Rate the background quality.
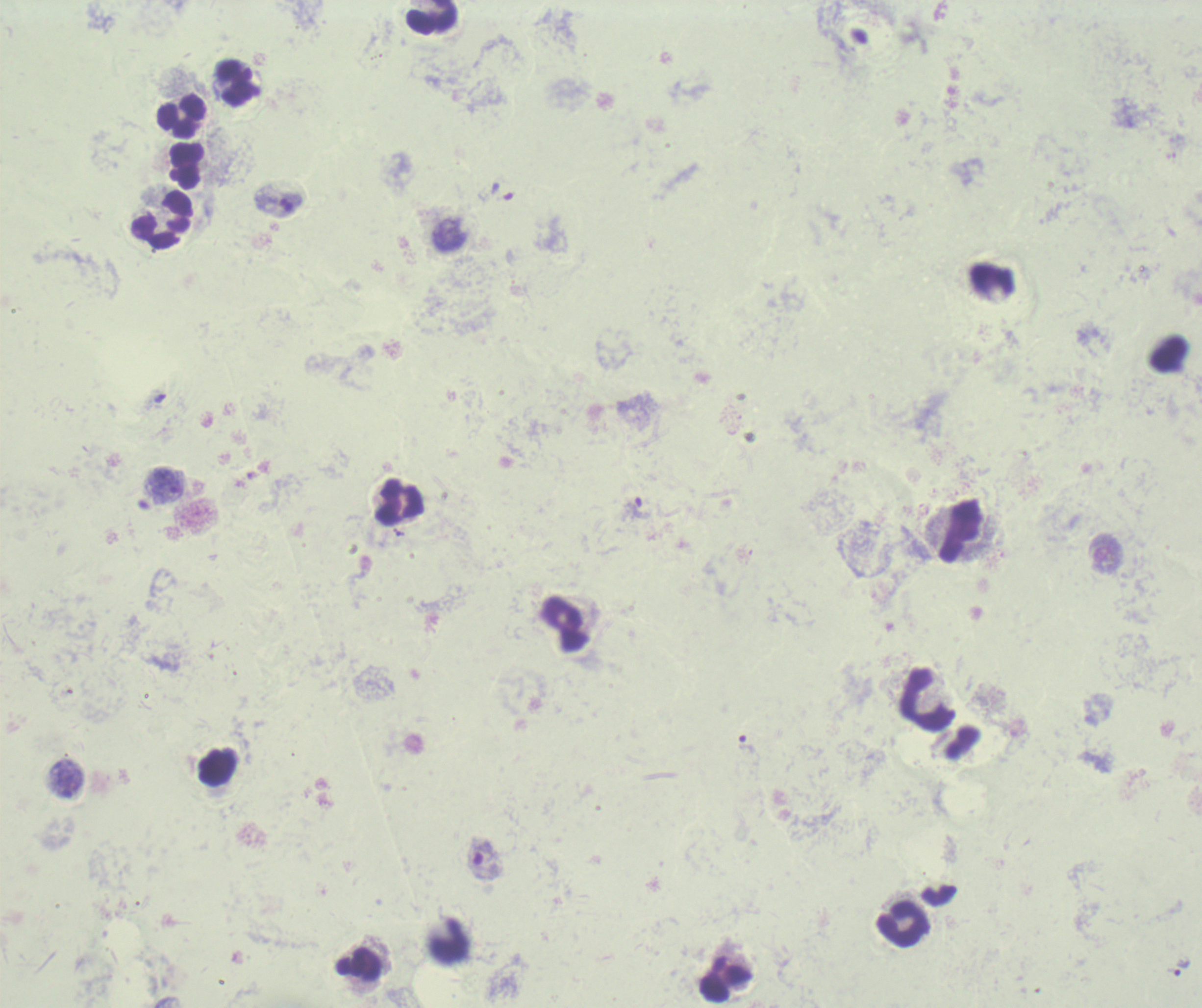

Poor.

Approximate centers as (x, y) in pixels.
Summary:
  - Leukocyte locations: (432, 17), (237, 83), (181, 118), (187, 166), (162, 221), (400, 502), (960, 531), (564, 624), (926, 701), (218, 768), (902, 925), (449, 940), (359, 965), (726, 980)
  - Trophozoite locations: (167, 485), (637, 509), (747, 745), (67, 779), (483, 858), (1181, 967)
  - Field of view: one from this slide
  - Stain: Romanowsky
  - Image size: 1202×1008 pixels
  - Context: previously used in an actual diagnosis
  - Magnification: 100x
  - Preparation: thick blood film
  - Result: Plasmodium parasites identified